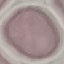 Malaria status: uninfected. Thin smear of blood. Automatically extracted cell patch, resized to 64 × 64 pixels. Giemsa-stained preparation. Photographed with a smartphone camera at the microscope eyepiece.